Report the malaria status of this cell.
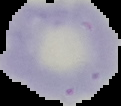

Uninfected.

{
  "image_type": "cell region segmented out of the field of view; surrounding area masked to black",
  "preparation": "thin blood smear",
  "image_size": "121×106 pixels"
}